Name the parasite shown.
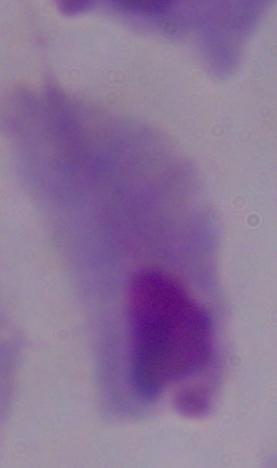

This is a trichomonad.

1000x magnification. Photomicrograph.